Assess this cell for malaria.
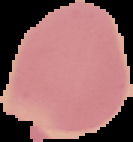
It is uninfected.

Summary:
  - Preparation: thin blood film
  - Image type: segmented cell region with the area outside set to black
  - Image size: 133×142 pixels